Name the cell type shown.
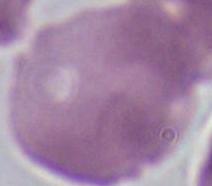

An erythrocyte.

Captured at 1000x magnification. Photomicrograph.